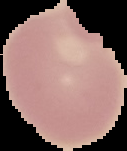
preparation = thin blood film
image size = 127×151 pixels
image type = segmented cell region with the area outside set to black
result = negative for malaria parasites